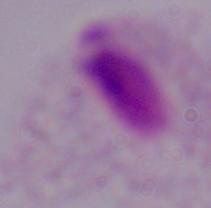

Summary:
  - Modality: photomicrograph
  - Identification: trichomonad
  - Magnification: 1000x